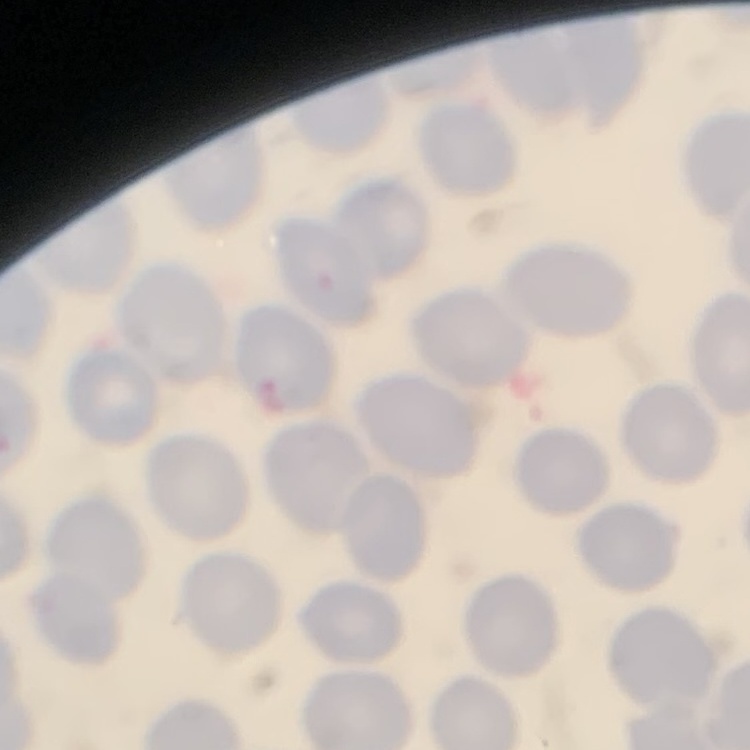
Summary:
  - Erythrocyte morphology: no rouleaux formation
  - Preparation: thin blood smear
  - Image type: square crop of a larger photomicrograph
  - Stain: Field's or Giemsa